Assess this cell for malaria.
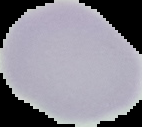
Uninfected.

Summary:
  - Preparation: thin blood smear
  - Image size: 142×127 pixels
  - Image type: segmented cell region on a black background